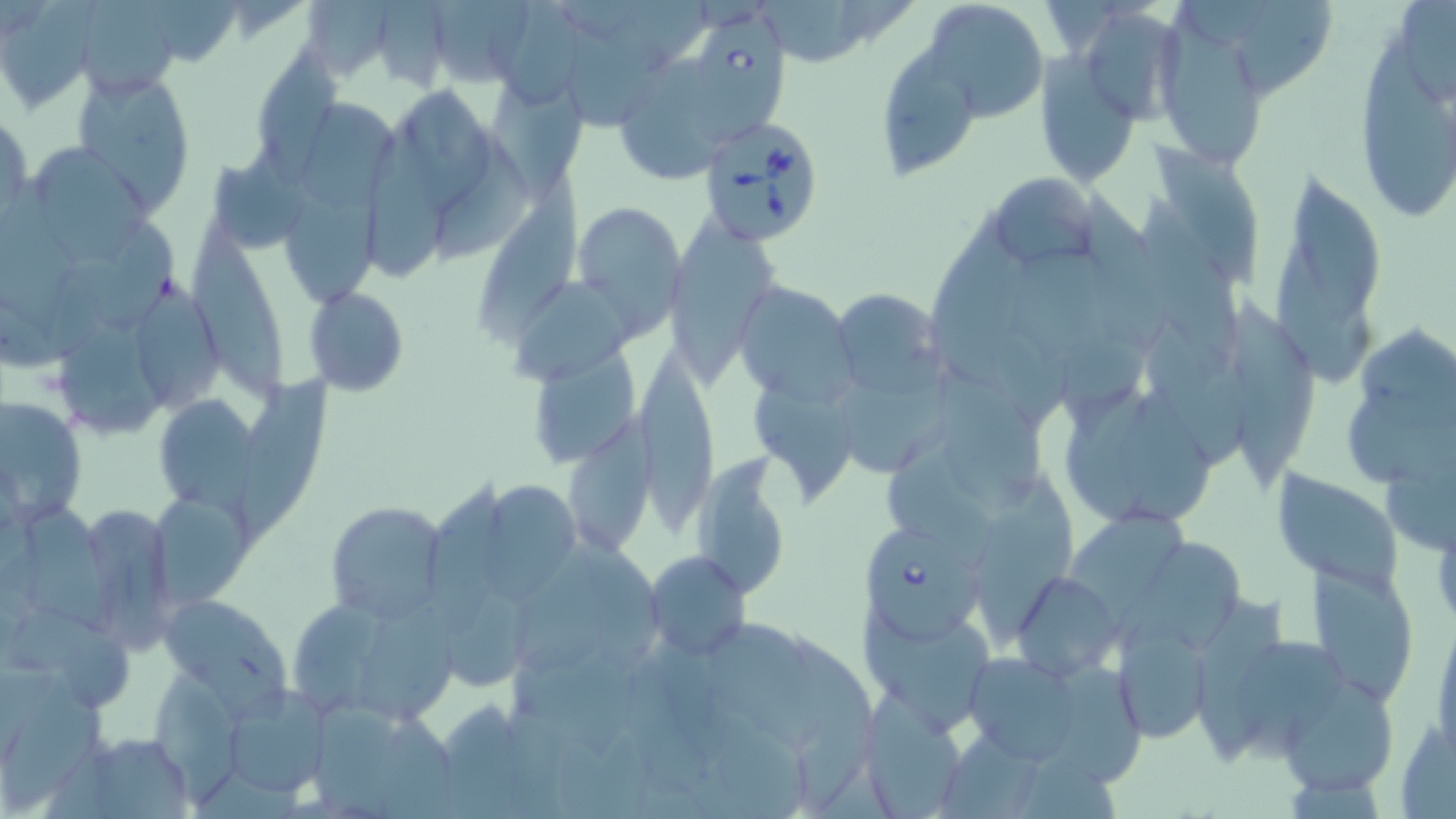
{
  "slide_level_diagnosis": "Babesia divergens",
  "uninfected_red_blood_cell_locations": "approximate bounding boxes as (x1,y1)-(x2,y2) corner pairs in pixels: (479,0)-(585,109), (921,0)-(1050,119), (1159,0)-(1267,164), (1237,0)-(1332,101), (67,1)-(188,99), (434,1)-(535,88), (306,2)-(396,81), (0,4)-(96,114), (552,5)-(652,121), (1350,7)-(1454,230), (1084,9)-(1198,119), (882,49)-(987,179), (257,50)-(345,189), (1034,52)-(1145,192), (626,56)-(724,179), (70,68)-(197,210), (409,83)-(497,215), (492,83)-(590,195), (293,94)-(402,214), (0,108)-(32,230), (368,126)-(446,285), (429,126)-(536,263), (1147,137)-(1260,292), (36,141)-(155,269), (1265,164)-(1389,380), (988,171)-(1097,269), (479,177)-(590,337), (0,179)-(73,345), (281,182)-(384,305), (1138,192)-(1247,360), (1082,195)-(1179,347), (572,200)-(686,325), (933,205)-(1037,387), (191,217)-(291,405), (664,223)-(783,386), (1007,249)-(1127,363), (138,268)-(231,414), (513,279)-(640,387), (736,281)-(854,403), (839,287)-(949,395), (307,288)-(411,397), (1219,295)-(1317,486), (1147,314)-(1253,473), (56,318)-(169,434), (1362,320)-(1456,426), (536,340)-(643,469), (635,346)-(717,542), (831,353)-(980,477), (940,365)-(1043,512), (238,372)-(338,543), (748,378)-(861,499), (1057,382)-(1225,529), (1347,393)-(1456,494), (152,394)-(260,510), (0,396)-(87,524), (564,408)-(663,555), (884,436)-(992,564), (689,458)-(795,597), (1272,473)-(1401,589), (982,476)-(1075,636), (484,477)-(586,603), (430,479)-(511,621), (154,492)-(253,606), (12,493)-(120,634), (324,500)-(449,623), (1069,508)-(1197,624), (83,512)-(172,654), (512,530)-(618,674), (583,530)-(668,673), (1115,543)-(1251,656), (643,550)-(751,661), (1307,561)-(1418,705), (1011,571)-(1122,680), (443,583)-(537,686), (282,586)-(459,727), (1194,593)-(1294,767), (158,595)-(293,712), (5,603)-(140,706), (1431,610)-(1456,763), (853,613)-(1000,738), (1113,621)-(1211,745), (701,623)-(819,755), (781,623)-(880,815), (1237,640)-(1355,762), (953,647)-(1114,772), (1052,662)-(1144,787), (153,668)-(237,807), (1277,675)-(1402,799), (1,681)-(119,814), (223,687)-(331,799), (859,696)-(971,818), (443,700)-(532,819), (306,702)-(458,816), (711,711)-(814,819), (1394,722)-(1456,817), (942,728)-(1061,819), (74,731)-(195,818)",
  "babesia_divergens_infected_red_blood_cell_locations": "approximate bounding boxes as (x1,y1)-(x2,y2) corner pairs in pixels: (683,9)-(787,144), (697,116)-(826,246), (869,526)-(983,647)",
  "stain": "May-Grünwald-Giemsa",
  "preparation": "thin blood smear",
  "modality": "optical microscopy",
  "field_of_view": "single",
  "magnification": "1000x",
  "image_size": "1456×819 pixels"
}